Comment on the morphology of the erythrocytes.
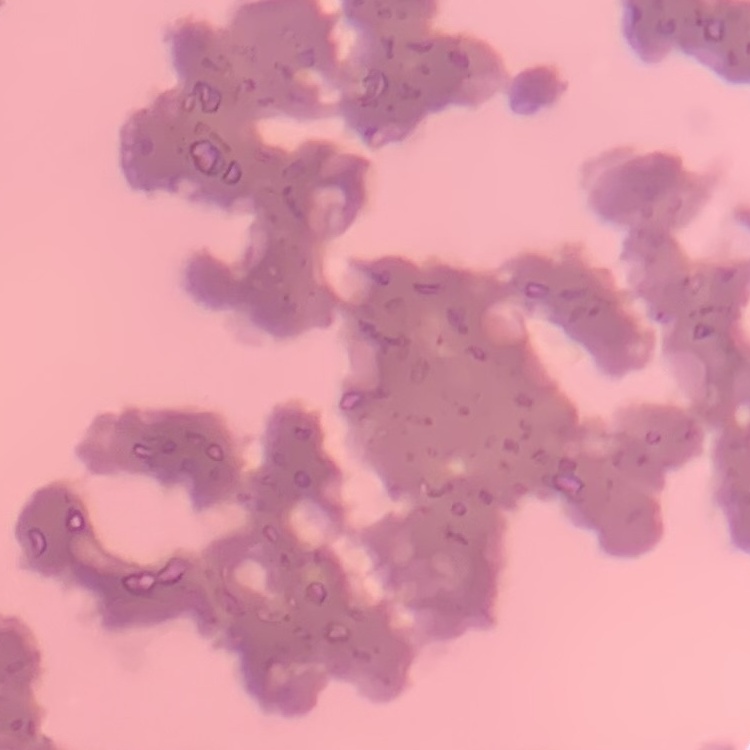

They show rouleaux formation.

Field's or Giemsa stain. Thin blood film. Square crop of a larger photomicrograph.